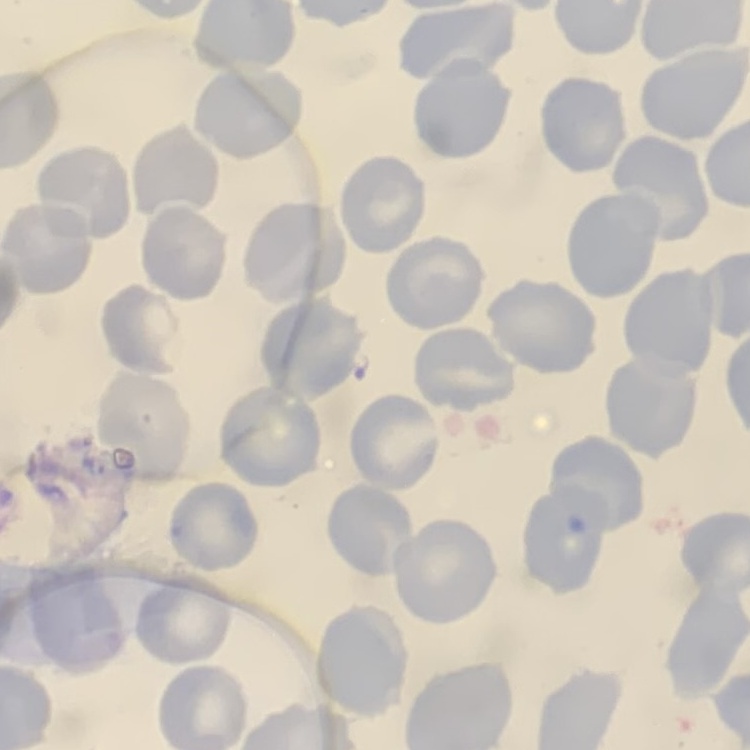

Summary:
  - Erythrocyte morphology: no rouleaux formation
  - Stain: Field's or Giemsa
  - Image type: one tile cut from a larger photomicrograph
  - Preparation: thin blood smear